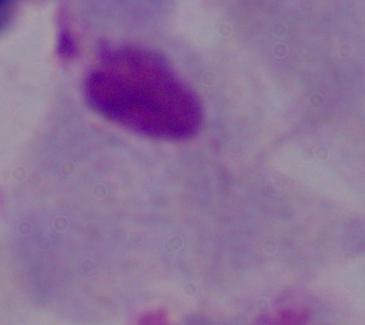

Micrograph. Captured at 1000x magnification. A trichomonad is seen.